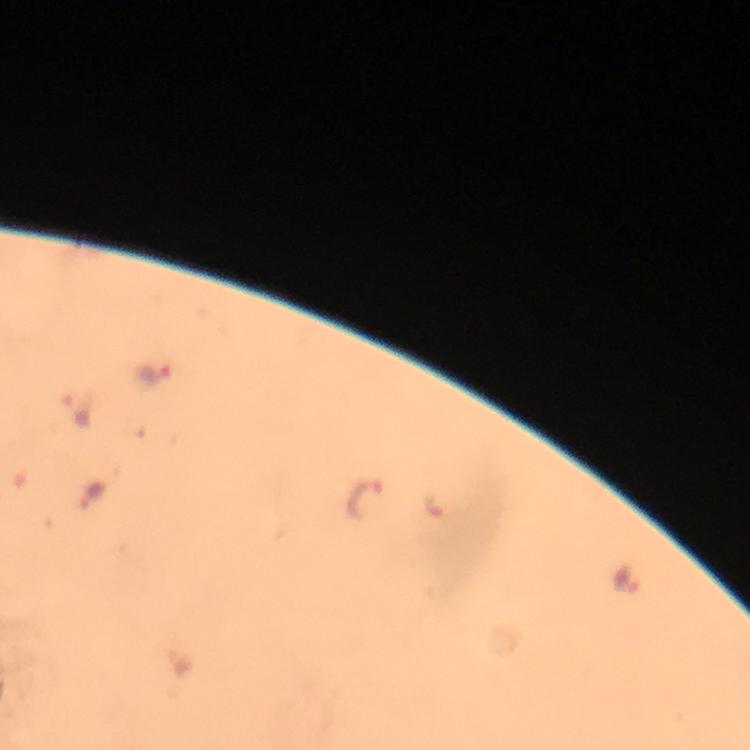
Approximate centers as [x, y] in pixels.
Summary:
  - Plasmodium parasite locations: [151, 373], [80, 411], [91, 496], [364, 500], [434, 506], [625, 581]
  - Preparation: thick smear
  - Capture: smartphone photograph through a microscope
  - Magnification: 100x
  - Image size: 750×750 pixels
  - Immersion oil: applied
  - Stain: Giemsa
  - Context: from a diagnostic examination for malaria
  - Cropped from: a single field of view